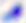

Summary:
  - Magnification: 400x
  - Modality: micrograph
  - Identification: Toxoplasma gondii